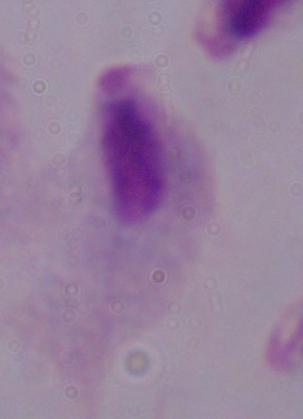

{
  "modality": "photomicrograph",
  "magnification": "1000x",
  "identification": "trichomonad"
}